State which parasite is depicted.
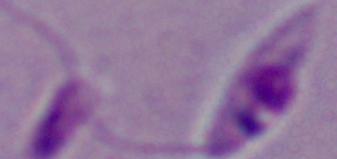
This is Leishmania.

Summary:
  - Modality: photomicrograph
  - Magnification: 1000x